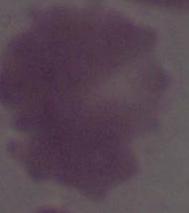 Micrograph. 1000x magnification. An erythrocyte is seen.